Report the malaria status.
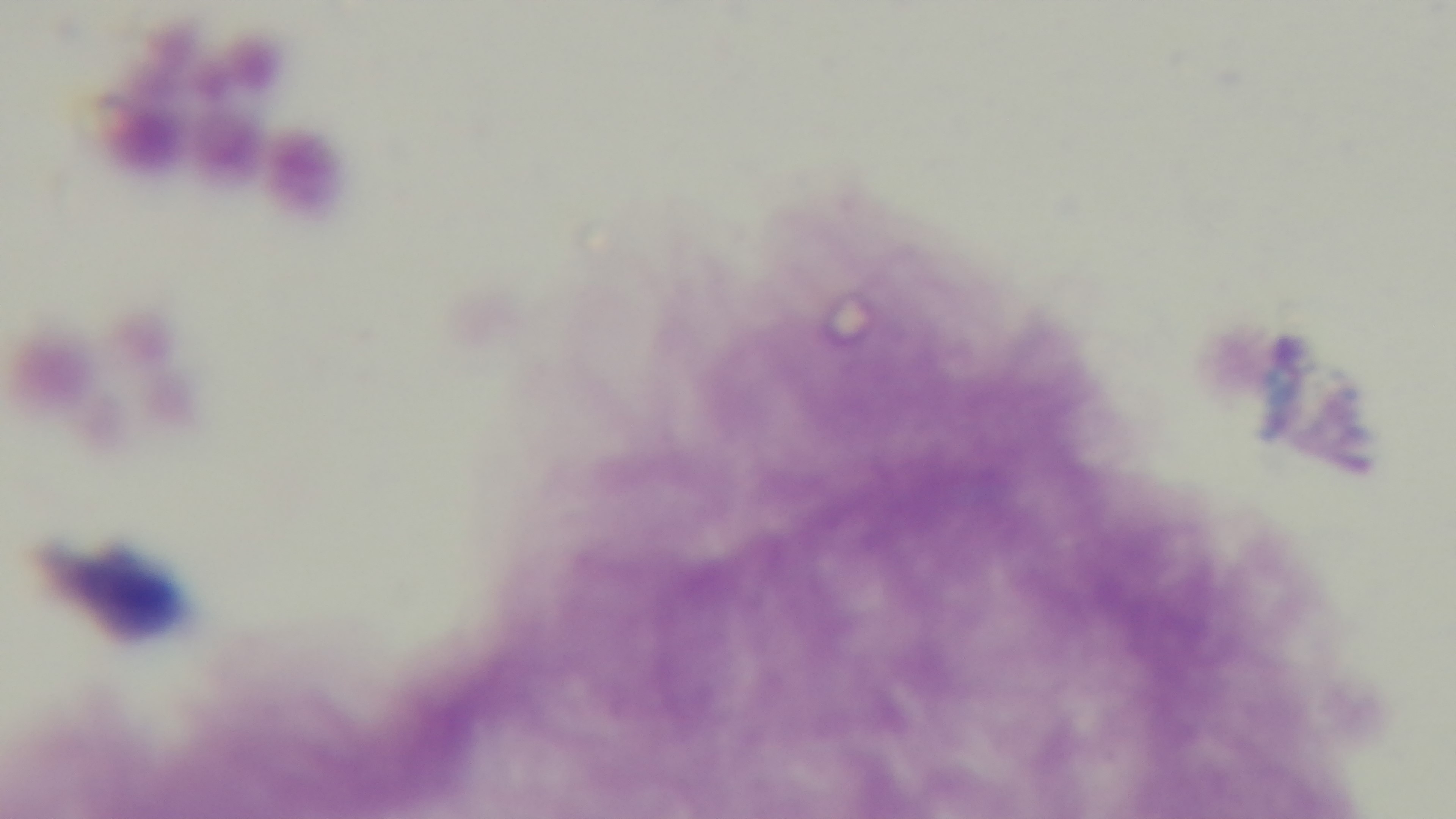
It is uninfected.

Mounted 4K digital camera. Oil-immersion objective, 100x. Single field of view. Photomicrograph. Preparation: thick smear. Giemsa stain.